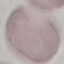

Result: no malaria parasites detected. Giemsa-stained preparation. Thin blood film. Automatically extracted cell patch, resized to 64 × 64 pixels. Photographed with a smartphone camera at the microscope eyepiece.